Identify the cell.
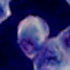

A leukocyte.

magnification: 1000x
modality: micrograph